Name the parasite shown.
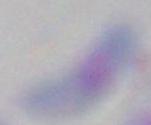
Toxoplasma gondii.

{
  "magnification": "1000x",
  "modality": "micrograph"
}